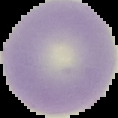

The area outside the segmented cell region is set to black. Image is 118×118 pixels. Malaria status: uninfected. From a thin blood film.